Evaluate for Plasmodium parasites.
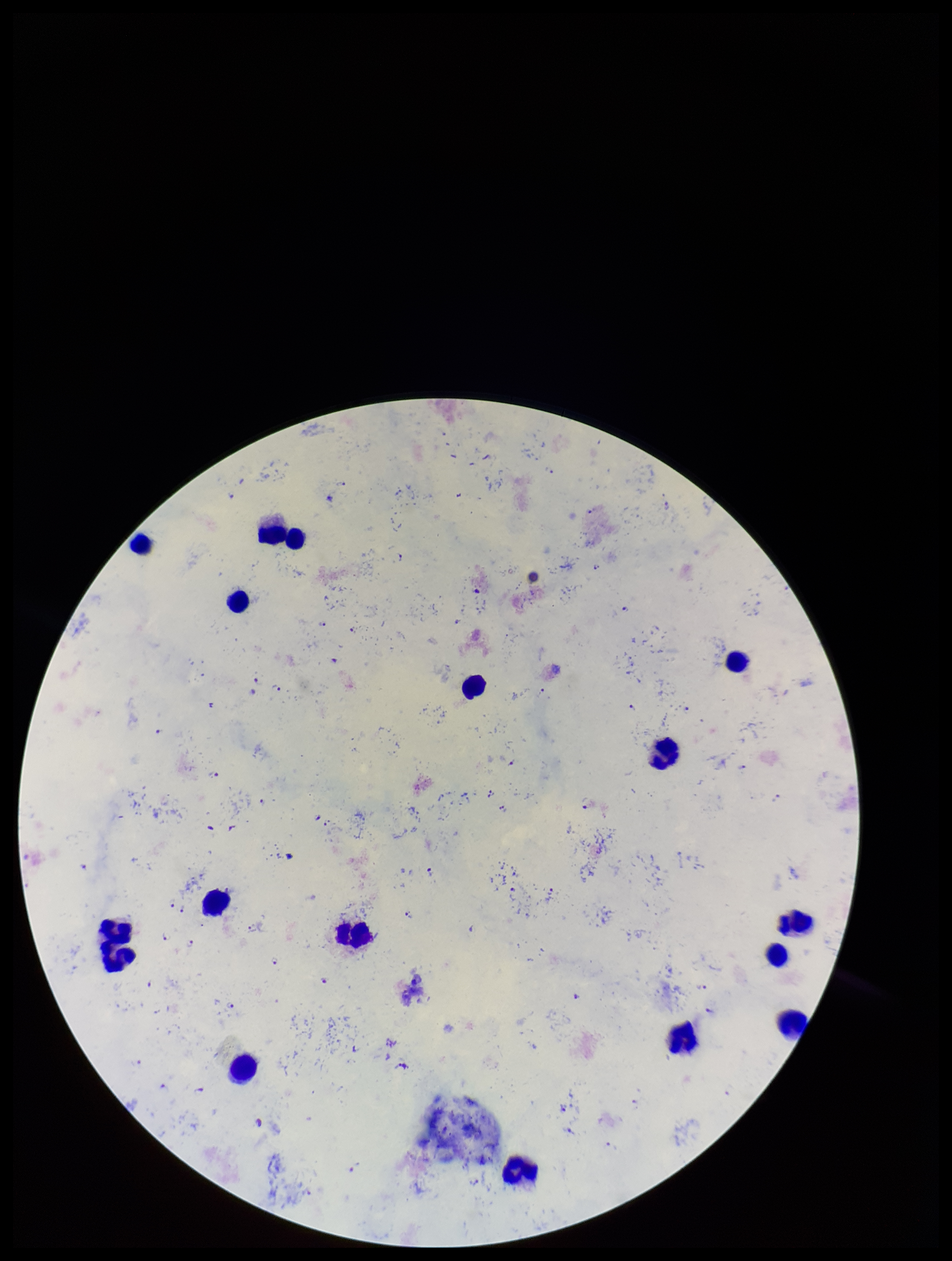
Seen.

Summary:
  - Stain: Giemsa
  - Leukocyte count: 16
  - Preparation: thick smear
  - Field of view: single
  - Species reported for this patient: Plasmodium falciparum
  - Image size: 952×1261 pixels
  - Parasite count: 54
  - Capture: smartphone photograph through the microscope eyepiece
  - Patient malaria status: infected